State the blood parasite species.
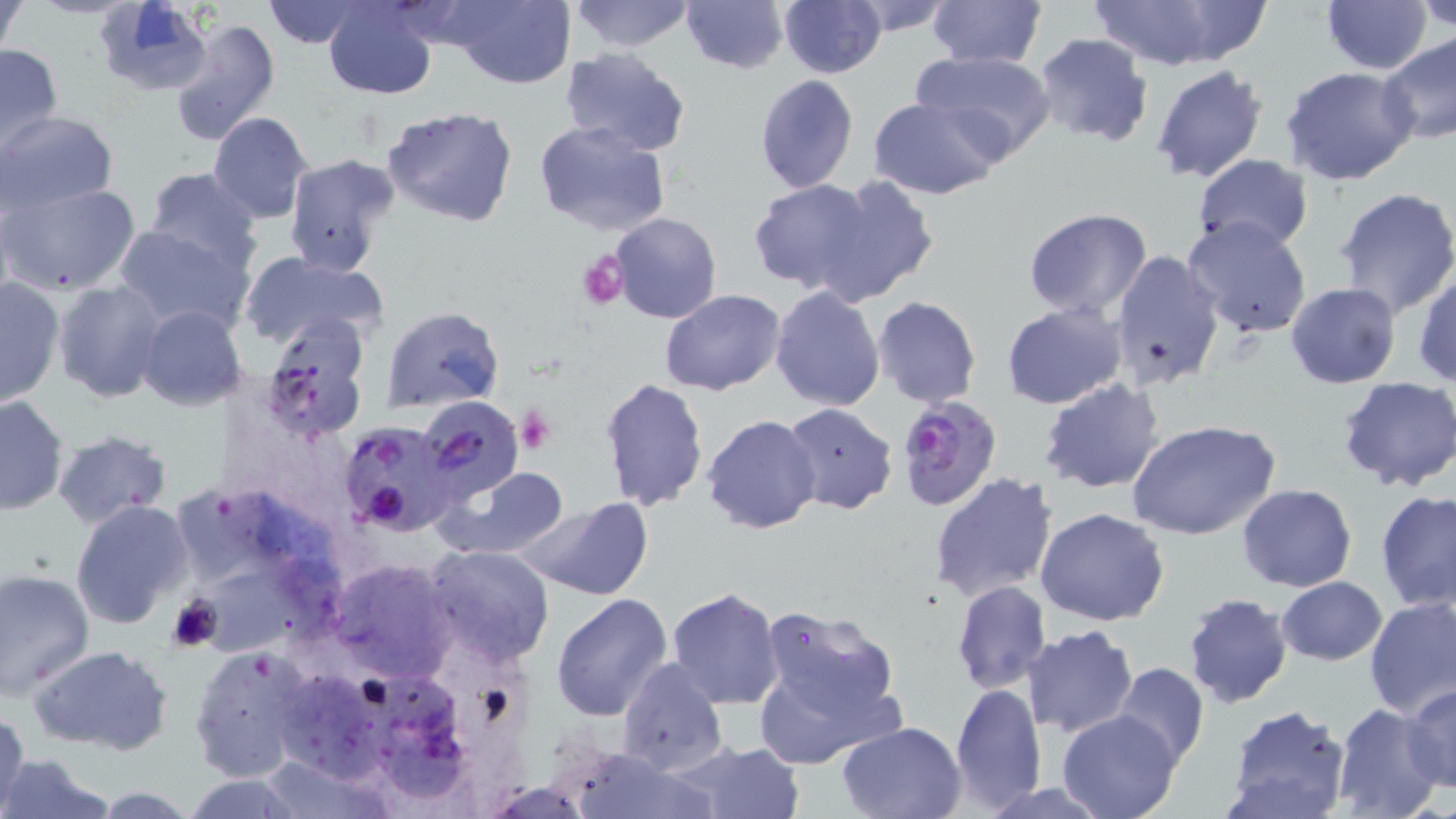
Plasmodium falciparum.

Approximate bounding boxes as named x1/y1/x2/y2 corners in pixels. Uninfected red blood cell locations: (x1=567, y1=0, x2=696, y2=54), (x1=681, y1=0, x2=789, y2=74), (x1=778, y1=0, x2=887, y2=79), (x1=840, y1=0, x2=960, y2=36), (x1=928, y1=0, x2=1047, y2=69), (x1=1086, y1=0, x2=1270, y2=70), (x1=1321, y1=0, x2=1434, y2=74), (x1=1417, y1=0, x2=1456, y2=32), (x1=1, y1=1, x2=26, y2=65), (x1=262, y1=1, x2=368, y2=48), (x1=323, y1=1, x2=440, y2=99), (x1=440, y1=1, x2=579, y2=89), (x1=94, y1=2, x2=217, y2=98), (x1=167, y1=17, x2=280, y2=146), (x1=1032, y1=34, x2=1154, y2=149), (x1=1378, y1=34, x2=1456, y2=147), (x1=0, y1=42, x2=64, y2=153), (x1=558, y1=47, x2=692, y2=160), (x1=910, y1=49, x2=1057, y2=161), (x1=1150, y1=64, x2=1269, y2=183), (x1=1282, y1=66, x2=1420, y2=186), (x1=753, y1=74, x2=860, y2=195), (x1=868, y1=97, x2=1005, y2=199), (x1=380, y1=104, x2=520, y2=228), (x1=0, y1=112, x2=119, y2=212), (x1=208, y1=112, x2=314, y2=225), (x1=532, y1=120, x2=673, y2=238), (x1=282, y1=153, x2=400, y2=278), (x1=1192, y1=153, x2=1313, y2=254), (x1=143, y1=167, x2=263, y2=277), (x1=815, y1=174, x2=942, y2=305), (x1=749, y1=179, x2=878, y2=295), (x1=2, y1=182, x2=143, y2=297), (x1=1333, y1=186, x2=1456, y2=321), (x1=1022, y1=209, x2=1152, y2=317), (x1=607, y1=213, x2=723, y2=325), (x1=1182, y1=216, x2=1312, y2=339), (x1=111, y1=223, x2=256, y2=338), (x1=1108, y1=248, x2=1226, y2=392), (x1=239, y1=249, x2=388, y2=352), (x1=1414, y1=268, x2=1455, y2=389), (x1=0, y1=277, x2=64, y2=408), (x1=53, y1=279, x2=167, y2=402), (x1=1285, y1=283, x2=1400, y2=388), (x1=770, y1=285, x2=885, y2=412), (x1=660, y1=290, x2=786, y2=396), (x1=871, y1=296, x2=981, y2=407), (x1=1001, y1=301, x2=1128, y2=410), (x1=137, y1=305, x2=248, y2=412), (x1=381, y1=306, x2=504, y2=414), (x1=258, y1=321, x2=370, y2=442), (x1=599, y1=376, x2=710, y2=513), (x1=1038, y1=378, x2=1166, y2=493), (x1=1337, y1=378, x2=1455, y2=493), (x1=0, y1=395, x2=67, y2=516), (x1=417, y1=396, x2=526, y2=503), (x1=783, y1=403, x2=898, y2=516), (x1=701, y1=413, x2=821, y2=535), (x1=1126, y1=418, x2=1281, y2=541), (x1=339, y1=420, x2=458, y2=537), (x1=51, y1=430, x2=173, y2=528), (x1=438, y1=465, x2=571, y2=562), (x1=929, y1=472, x2=1060, y2=602), (x1=1237, y1=483, x2=1357, y2=592), (x1=1375, y1=489, x2=1456, y2=612), (x1=524, y1=497, x2=654, y2=602), (x1=69, y1=500, x2=193, y2=631), (x1=1035, y1=508, x2=1169, y2=627), (x1=424, y1=545, x2=555, y2=668), (x1=328, y1=558, x2=458, y2=682), (x1=0, y1=568, x2=95, y2=697), (x1=1275, y1=577, x2=1388, y2=666), (x1=208, y1=578, x2=318, y2=656), (x1=952, y1=580, x2=1051, y2=693), (x1=665, y1=587, x2=784, y2=709), (x1=550, y1=593, x2=672, y2=720), (x1=1183, y1=594, x2=1293, y2=708), (x1=1364, y1=595, x2=1456, y2=719), (x1=755, y1=605, x2=903, y2=732), (x1=1022, y1=627, x2=1139, y2=737), (x1=188, y1=641, x2=320, y2=782), (x1=27, y1=644, x2=172, y2=755), (x1=616, y1=657, x2=728, y2=775), (x1=1112, y1=662, x2=1208, y2=770), (x1=949, y1=681, x2=1046, y2=811), (x1=1403, y1=685, x2=1456, y2=792), (x1=295, y1=688, x2=386, y2=776), (x1=370, y1=688, x2=469, y2=800), (x1=1330, y1=703, x2=1443, y2=819), (x1=1224, y1=707, x2=1350, y2=819), (x1=0, y1=708, x2=29, y2=818), (x1=1057, y1=710, x2=1182, y2=819), (x1=837, y1=720, x2=967, y2=817), (x1=673, y1=741, x2=804, y2=819), (x1=562, y1=746, x2=716, y2=819), (x1=2, y1=753, x2=113, y2=819), (x1=181, y1=776, x2=305, y2=816), (x1=976, y1=781, x2=1114, y2=818). Platelet locations: (x1=578, y1=251, x2=629, y2=311), (x1=513, y1=405, x2=556, y2=454), (x1=167, y1=595, x2=221, y2=653). Plasmodium falciparum-infected red blood cell locations: (x1=897, y1=393, x2=1004, y2=512). Thin blood smear. May-Grünwald-Giemsa stain. Light microscopy. Single field of view. Image is 1456×819 pixels. 1000x magnification.